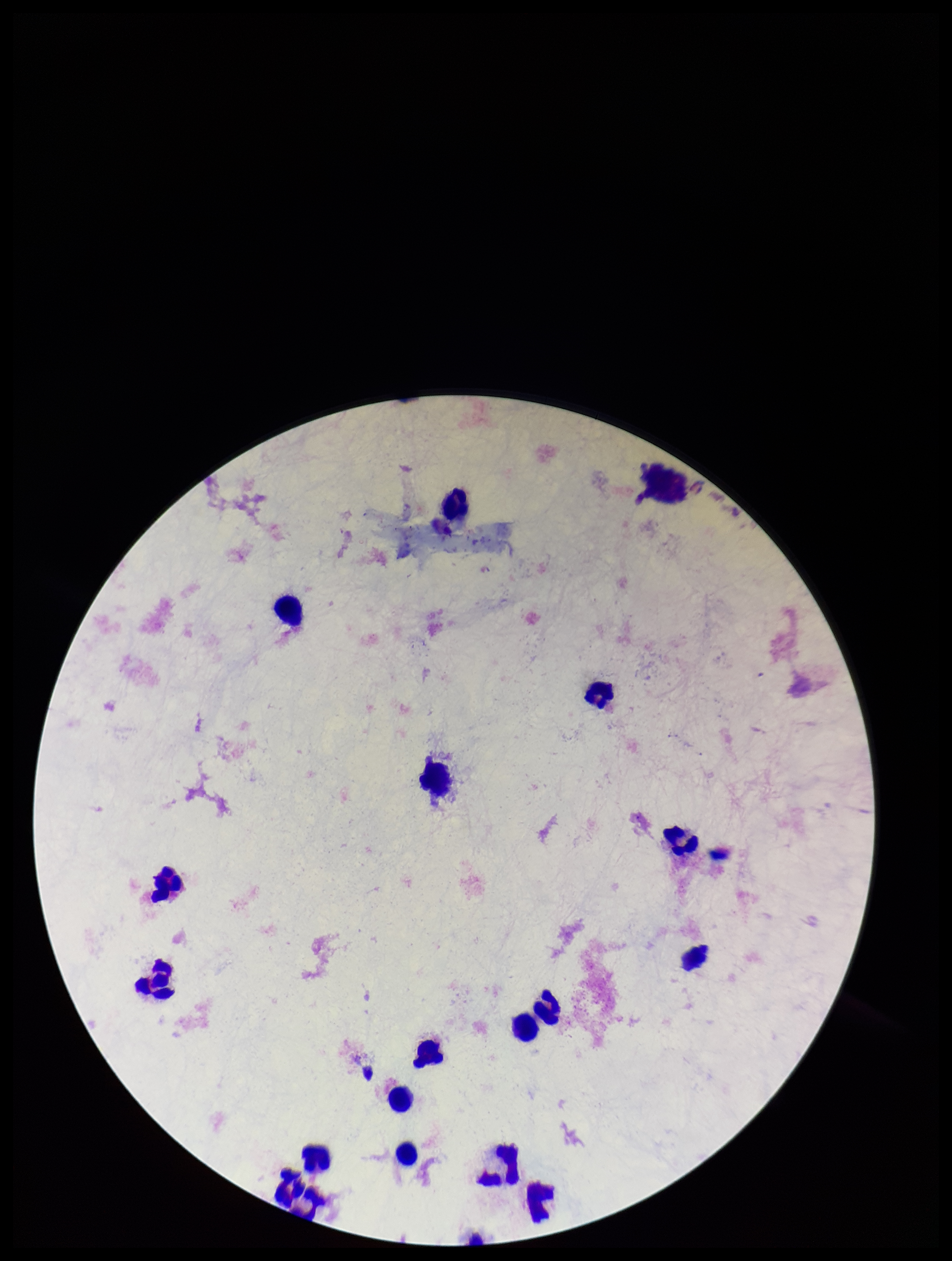

Stained with Giemsa. Parasite count: 0. Single field of view. Plasmodium parasites: none detected. Image is 952×1261 pixels. Patient malaria status: negative. Preparation: thick. Photographed through the microscope eyepiece with a smartphone camera. Leukocyte count: 17.